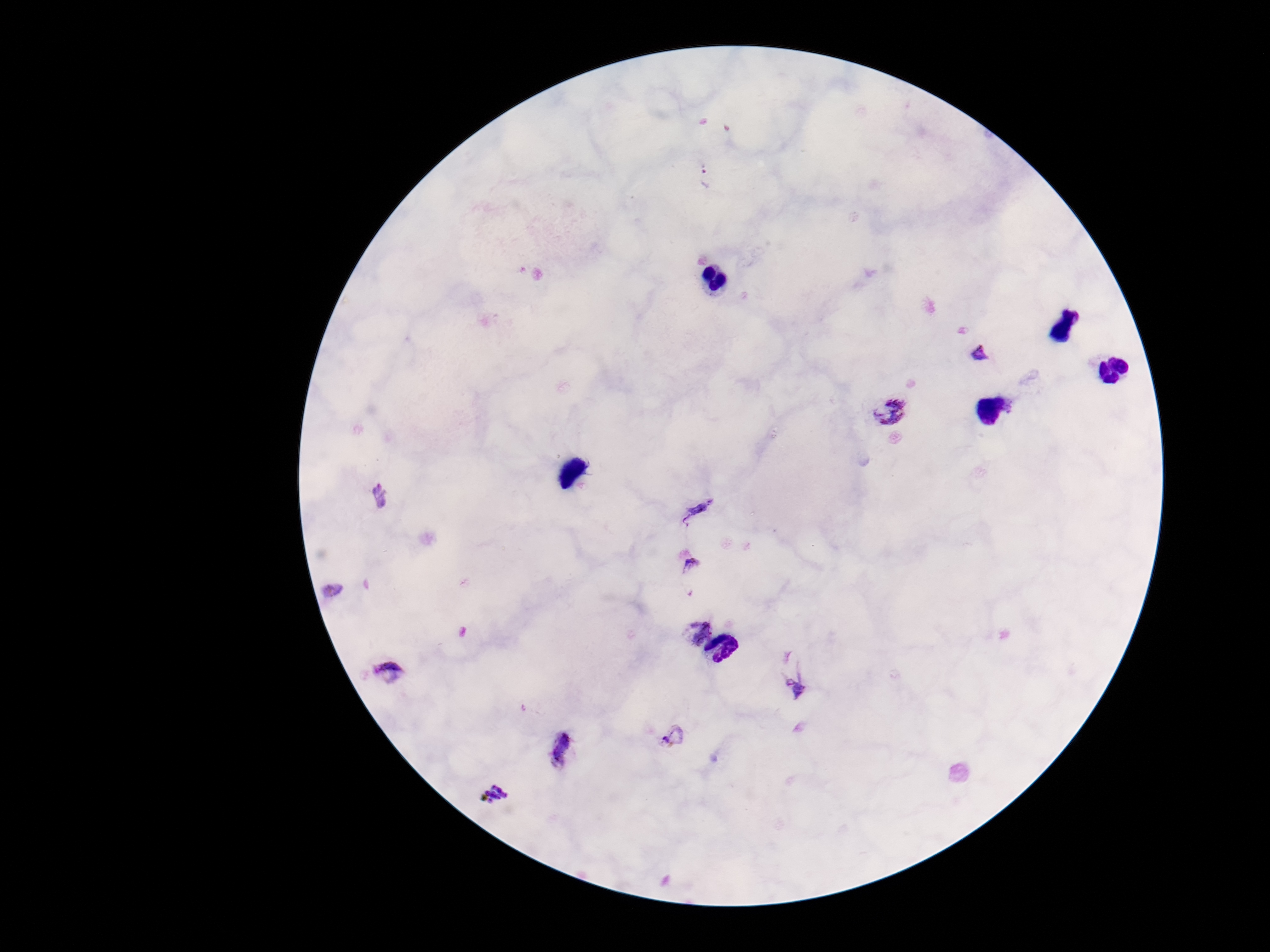
patient_malaria_status: positive
image_size: 1270×952 pixels
stain: Giemsa
plasmodium_parasite_locations: 'approximate object centers, in pixels from the top-left corner: (x=707, y=177), (x=979, y=354), (x=891, y=412), (x=380, y=497), (x=699, y=509), (x=695, y=574), (x=333, y=590), (x=696, y=632), (x=391, y=671), (x=798, y=682), (x=673, y=736), (x=562, y=750), (x=493, y=794)'
capture: smartphone camera through the microscope eyepiece
preparation: thick blood film
field_of_view: one from this slide
magnification: 100x